State which cell type is depicted.
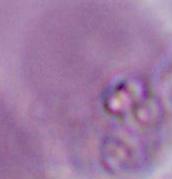

An erythrocyte.

Summary:
  - Magnification: 1000x
  - Modality: micrograph